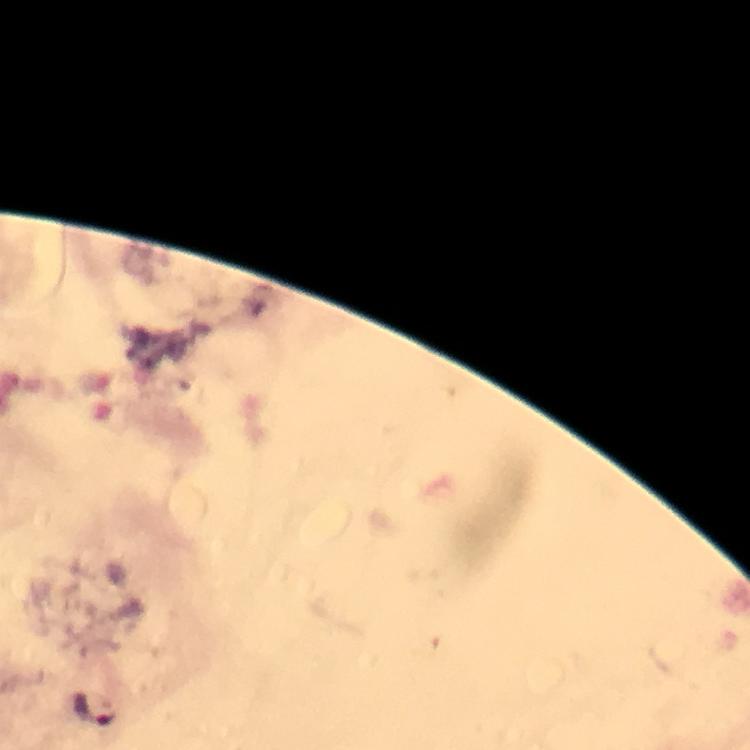

Approximate centers as {x, y} in pixels.
Summary:
  - Plasmodium parasite locations: {93, 710}
  - Image size: 750×750 pixels
  - Immersion oil: used
  - Stain: Giemsa
  - Context: from a malaria diagnostic workup
  - Magnification: 100x
  - Preparation: thick blood film
  - Capture: smartphone camera through the microscope
  - Cropped from: one field of view